State which cell type is depicted.
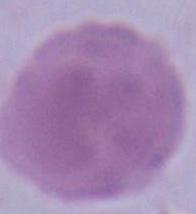
An erythrocyte.

1000x magnification. Photomicrograph.